Report the malaria status of this cell.
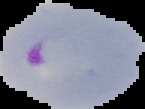

It is parasitized.

From a thin blood film. Segmented cell region on a black background. Image is 145×109 pixels.